Comment on the morphology of the erythrocytes.
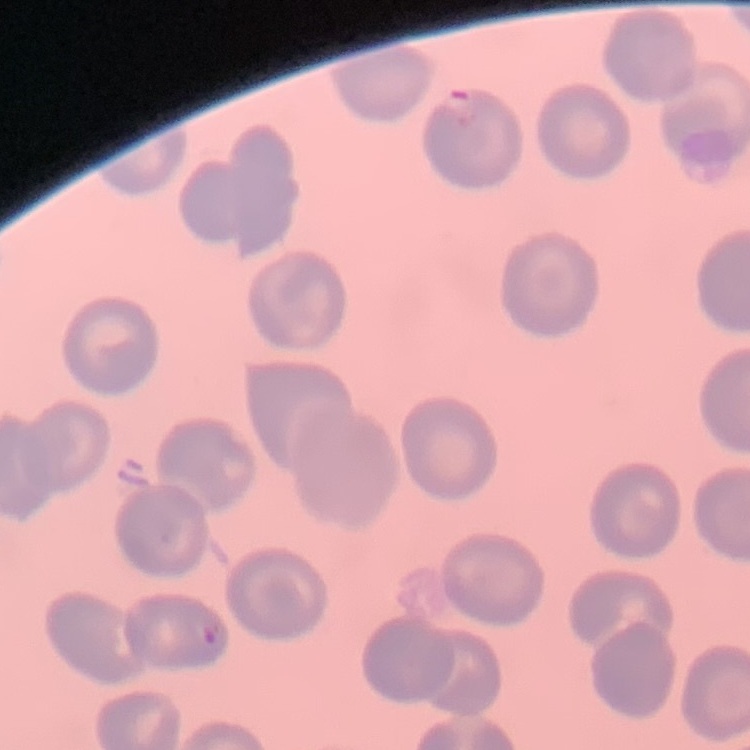

They show no rouleaux formation.

Stained with either Field's or Giemsa. Thin blood film. Square crop of a larger photomicrograph.